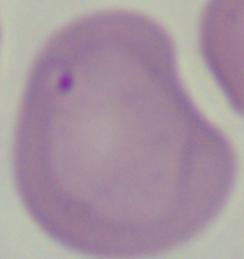
A Babesia parasite is seen. 1000x magnification. Photomicrograph.